Give the position of every malaria parasite.
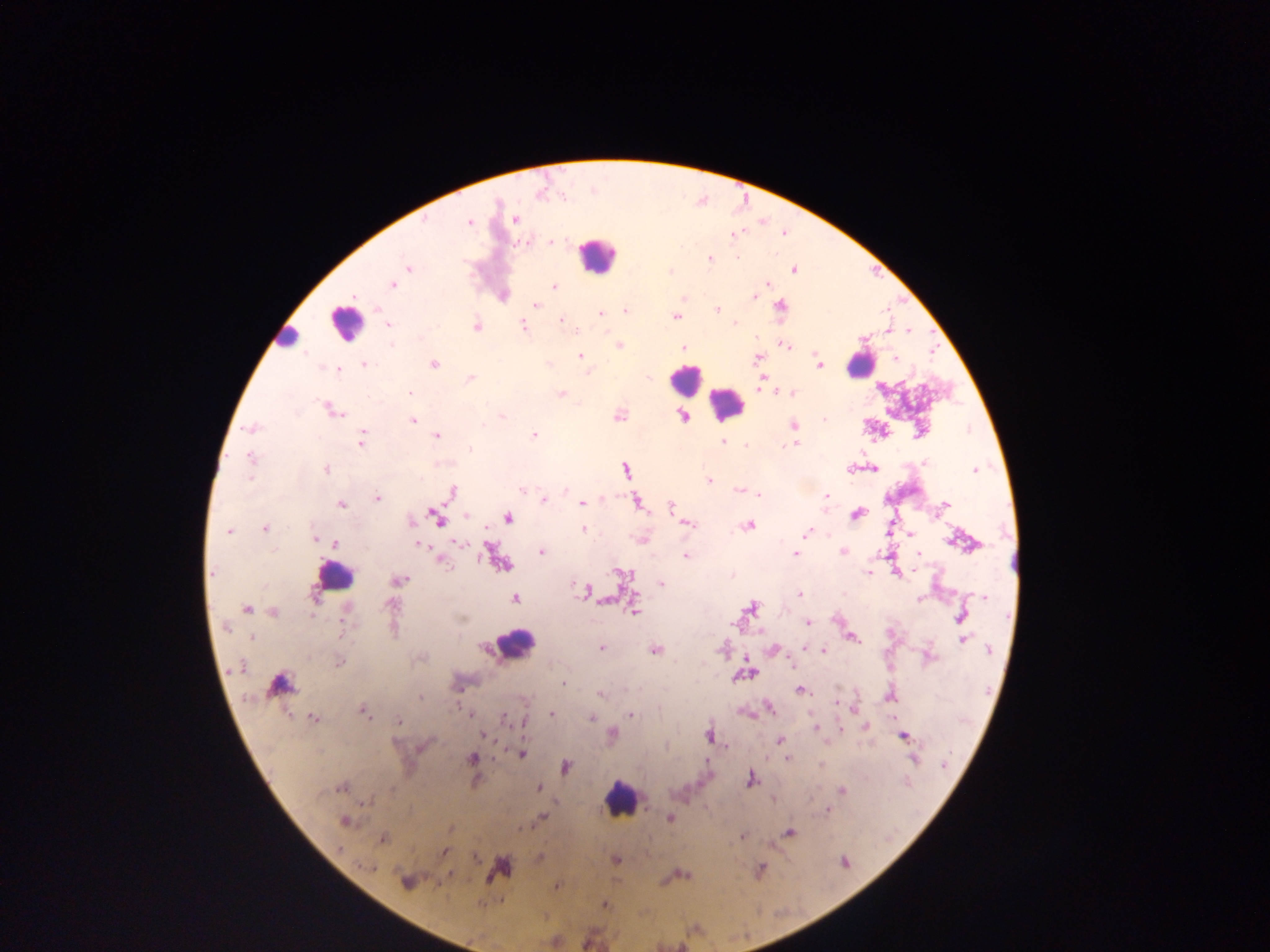

Approximate centers as x y in pixels.
Malaria parasites: 515 219; 469 222; 735 235; 553 241; 708 259; 408 268; 794 269; 767 284; 393 285; 554 287; 758 289; 754 296; 536 304; 780 306; 626 310; 717 310; 601 314; 675 316; 561 319; 734 323; 388 325; 476 326; 523 326; 619 345; 786 345; 684 348; 580 356; 757 358; 895 359; 433 364; 819 364; 365 365; 339 370; 470 378; 409 393; 791 393; 561 394; 331 410; 618 415; 503 416; 684 417; 824 420; 413 421; 793 425; 483 426; 252 428; 534 435; 436 436; 361 440; 724 443; 794 444; 745 445; 471 449; 250 457; 925 462; 325 469; 625 469; 874 469; 975 469; 249 477; 708 480; 565 490; 739 490; 522 491; 453 492; 754 492; 759 494; 826 496; 377 498; 545 500; 637 502; 582 503; 340 504; 945 504; 671 507; 857 514; 467 516; 436 517; 507 518; 411 522; 689 523; 749 525; 265 529; 583 529; 228 531; 807 532; 910 533; 315 538; 641 539; 459 543; 335 544; 421 545; 425 549; 843 552; 541 553; 918 553; 796 554; 686 556; 443 563; 501 563; 213 572; 868 573; 621 574; 399 579; 662 584; 585 592; 800 594; 983 596; 515 598; 920 598; 390 605; 751 608; 247 609; 274 611; 633 612; 961 617; 808 623; 226 627; 852 637; 253 638; 963 639; 601 648; 774 649; 805 649; 655 650; 990 650; 823 651; 930 657; 338 663; 744 674; 563 683; 279 684; 800 690; 600 694; 420 696; 889 697; 837 703; 770 708; 363 712; 467 713; 551 714; 630 715; 591 717; 504 718; 314 719; 398 721; 815 728; 613 733; 484 734; 709 736; 903 737; 780 740; 521 753; 472 758; 788 759; 915 759; 944 765; 567 767; 751 779; 341 788; 539 788; 842 791; 827 810; 541 818; 669 818; 344 821; 790 832; 742 836; 382 839; 445 852; 616 860; 845 863; 367 866; 406 882; 557 886; 605 904.

{
  "image_size": "1270×952 pixels",
  "capture": "mobile-phone photograph through a microscope",
  "preparation": "thick blood smear",
  "country": "Ghana",
  "leukocyte_locations": "approximate centers as x y in pixels: 597 255; 345 324; 861 364; 686 377; 727 405; 333 576; 513 645; 620 798",
  "field_of_view": "single"
}